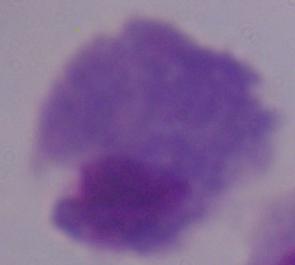

modality: micrograph
identification: trichomonad
magnification: 1000x